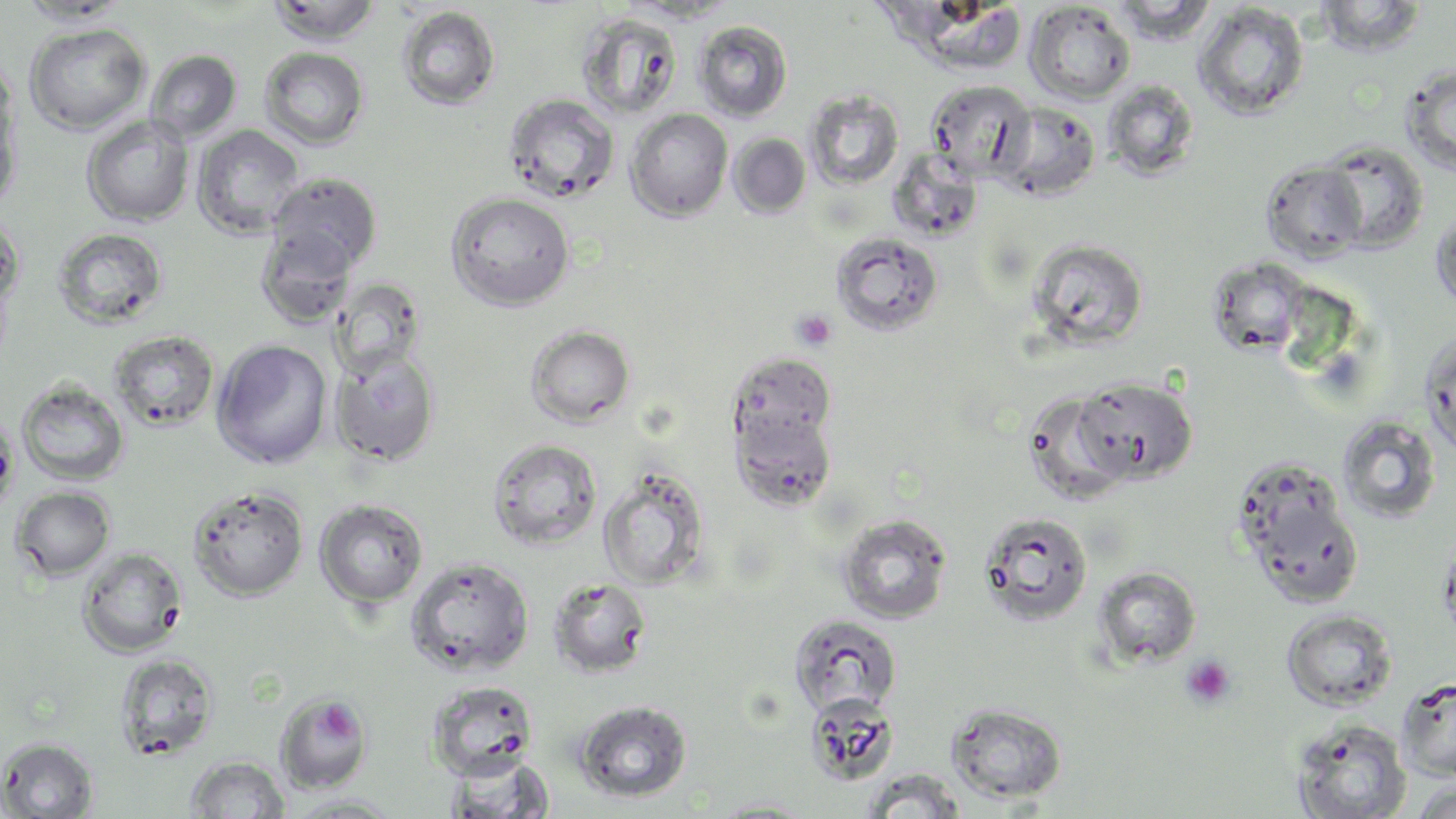
slide-level diagnosis = negative for blood parasites
field of view = one of a larger specimen
preparation = thin blood smear
image size = 1456×819 pixels
platelet locations = approximate bounding boxes as (x1,y1)-(x2,y2) corner pairs in pixels: (792,310)-(836,350), (1180,654)-(1237,710), (320,702)-(358,742)
magnification = 1000x
uninfected red blood cell locations = approximate bounding boxes as (x1,y1)-(x2,y2) corner pairs in pixels: (266,0)-(382,46), (1109,0)-(1216,44), (1314,0)-(1426,57), (16,1)-(130,25), (1025,2)-(1135,104), (1193,3)-(1310,120), (396,6)-(501,111), (577,12)-(683,121), (692,20)-(793,121), (23,22)-(151,135), (258,47)-(370,150), (145,49)-(242,144), (0,56)-(20,167), (1400,63)-(1456,176), (925,79)-(1034,179), (1103,79)-(1201,180), (804,90)-(904,190), (503,93)-(620,204), (1,95)-(20,216), (993,102)-(1100,201), (626,109)-(733,222), (81,115)-(195,227), (193,125)-(305,239), (729,133)-(811,218), (1317,139)-(1429,253), (888,150)-(983,241), (1261,160)-(1369,263), (267,172)-(383,274), (445,191)-(575,310), (1430,206)-(1456,313), (0,212)-(24,328), (53,227)-(168,330), (255,227)-(358,328), (830,230)-(944,337), (1027,238)-(1148,351), (1207,257)-(1311,357), (329,279)-(425,378), (525,325)-(636,428), (1419,329)-(1456,460), (109,330)-(220,431), (212,339)-(333,469), (329,348)-(441,466), (729,352)-(836,449), (1073,377)-(1198,486), (15,379)-(130,486), (1022,390)-(1136,505), (732,407)-(838,511), (0,414)-(19,519), (1337,416)-(1441,524), (487,438)-(603,550), (597,467)-(709,591), (1237,475)-(1364,610), (187,485)-(309,602), (11,486)-(115,581), (314,499)-(428,608), (978,511)-(1094,627), (837,514)-(952,624), (77,547)-(187,658), (405,556)-(535,677), (1092,566)-(1201,669), (548,577)-(653,678), (1282,609)-(1397,711), (789,614)-(902,718), (114,653)-(219,761), (1396,676)-(1456,781), (426,681)-(540,780), (275,692)-(373,794), (805,693)-(900,786), (574,699)-(692,803), (947,702)-(1067,803), (1291,719)-(1412,819), (0,737)-(98,818), (444,754)-(556,818), (185,755)-(290,818), (860,769)-(969,818), (1411,779)-(1456,818), (283,794)-(404,817), (709,798)-(821,817)
stain = May-Grünwald-Giemsa
modality = light microscopy